Describe the morphology of the erythrocytes.
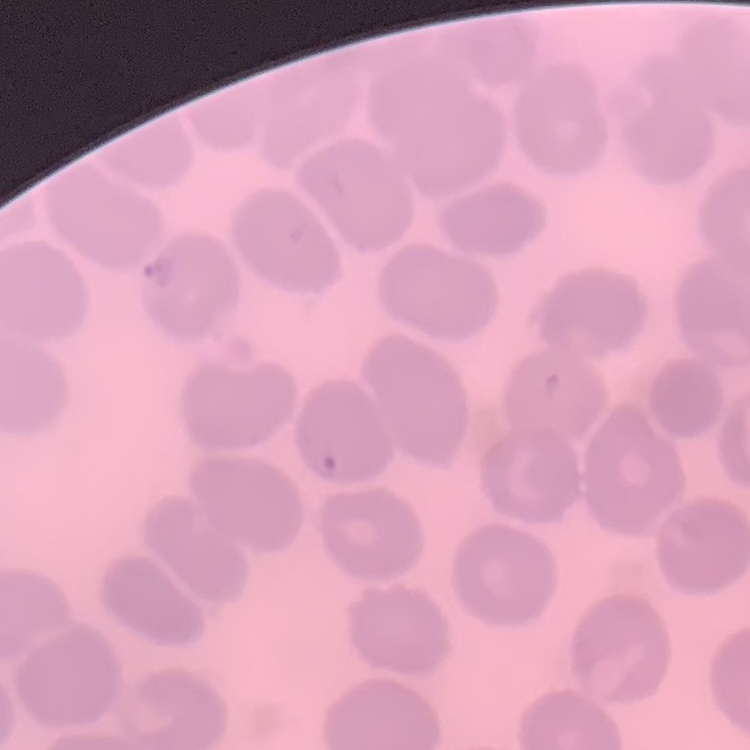

They show no rouleaux formation.

Stained with either Field's or Giemsa. Square crop of a larger photomicrograph. Thin blood smear.